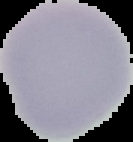

Image is 133×142 pixels. From a thin blood film. Cell region segmented out of the field of view; the surrounding area is masked to black. Malaria status: uninfected.